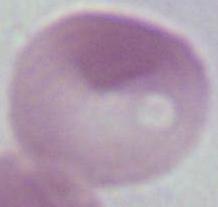
Summary:
  - Identification: erythrocyte
  - Modality: micrograph
  - Magnification: 1000x